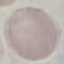
Result: no malaria parasites detected. Acquired by smartphone through the microscope eyepiece. Automatically extracted cell patch, resized to 64 × 64 pixels. Thin smear of blood. Giemsa-stained preparation.